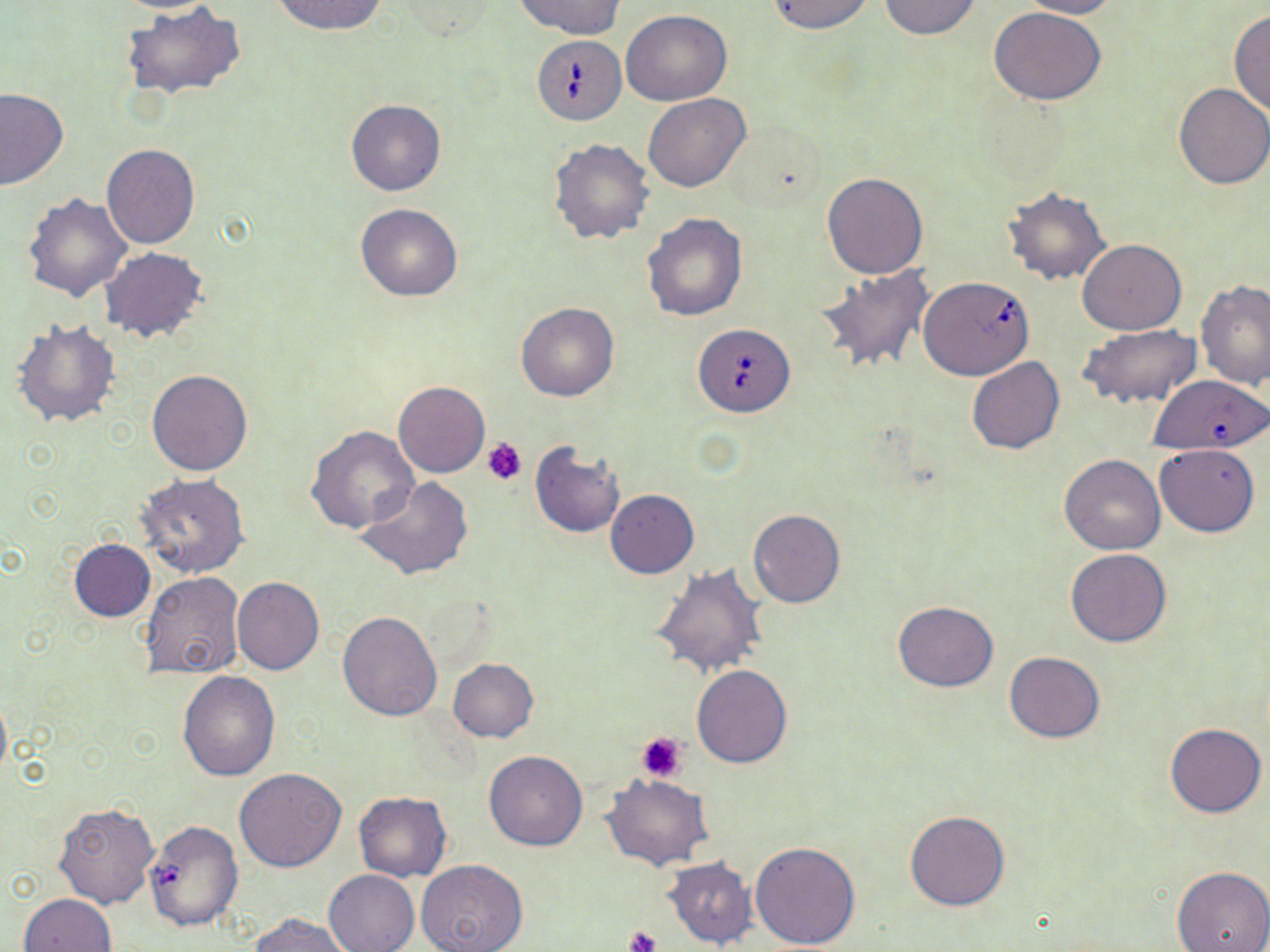

slide_level_diagnosis: Babesia divergens
stain: May-Grünwald-Giemsa
modality: optical microscopy
image_size: 1270×952 pixels
platelet_locations: 'approximate bounding boxes as named x1/y1/x2/y2 corners in pixels: (x1=484, y1=438, x2=528, y2=485), (x1=637, y1=732, x2=688, y2=781), (x1=626, y1=925, x2=662, y2=952)'
babesia_divergens_infected_red_blood_cell_locations: 'approximate bounding boxes as named x1/y1/x2/y2 corners in pixels: (x1=531, y1=35, x2=625, y2=124), (x1=920, y1=277, x2=1033, y2=380), (x1=694, y1=324, x2=796, y2=416), (x1=1147, y1=378, x2=1270, y2=457), (x1=145, y1=822, x2=243, y2=932)'
field_of_view: one of a larger specimen
uninfected_red_blood_cell_locations: 'approximate bounding boxes as named x1/y1/x2/y2 corners in pixels: (x1=106, y1=0, x2=226, y2=13), (x1=271, y1=0, x2=388, y2=36), (x1=517, y1=0, x2=624, y2=39), (x1=767, y1=0, x2=875, y2=35), (x1=877, y1=0, x2=983, y2=41), (x1=1017, y1=0, x2=1122, y2=19), (x1=119, y1=1, x2=247, y2=101), (x1=388, y1=1, x2=499, y2=41), (x1=990, y1=7, x2=1107, y2=106), (x1=621, y1=9, x2=731, y2=105), (x1=1229, y1=10, x2=1270, y2=118), (x1=1173, y1=83, x2=1270, y2=189), (x1=0, y1=88, x2=67, y2=190), (x1=643, y1=93, x2=750, y2=193), (x1=346, y1=99, x2=447, y2=196), (x1=548, y1=137, x2=655, y2=244), (x1=101, y1=144, x2=200, y2=249), (x1=822, y1=172, x2=928, y2=279), (x1=1001, y1=185, x2=1111, y2=285), (x1=23, y1=192, x2=132, y2=303), (x1=354, y1=203, x2=463, y2=301), (x1=642, y1=212, x2=747, y2=320), (x1=1077, y1=238, x2=1186, y2=335), (x1=100, y1=247, x2=208, y2=342), (x1=815, y1=265, x2=935, y2=376), (x1=1195, y1=280, x2=1270, y2=392), (x1=516, y1=303, x2=618, y2=402), (x1=11, y1=318, x2=122, y2=428), (x1=1081, y1=322, x2=1203, y2=408), (x1=967, y1=357, x2=1064, y2=454), (x1=147, y1=369, x2=253, y2=476), (x1=392, y1=381, x2=489, y2=478), (x1=306, y1=424, x2=419, y2=534), (x1=529, y1=442, x2=625, y2=537), (x1=1155, y1=443, x2=1259, y2=536), (x1=1060, y1=455, x2=1165, y2=554), (x1=137, y1=473, x2=249, y2=578), (x1=357, y1=477, x2=475, y2=581), (x1=606, y1=490, x2=699, y2=578), (x1=748, y1=509, x2=844, y2=608), (x1=68, y1=538, x2=156, y2=622), (x1=1066, y1=548, x2=1171, y2=646), (x1=651, y1=563, x2=768, y2=679), (x1=139, y1=571, x2=246, y2=680), (x1=231, y1=576, x2=324, y2=675), (x1=892, y1=601, x2=999, y2=691), (x1=337, y1=610, x2=443, y2=721), (x1=1003, y1=651, x2=1105, y2=743), (x1=447, y1=657, x2=538, y2=741), (x1=691, y1=665, x2=793, y2=768), (x1=177, y1=670, x2=281, y2=780), (x1=1165, y1=722, x2=1266, y2=818), (x1=483, y1=750, x2=588, y2=851), (x1=234, y1=768, x2=347, y2=872), (x1=602, y1=774, x2=711, y2=870), (x1=353, y1=792, x2=452, y2=882), (x1=51, y1=801, x2=159, y2=908), (x1=905, y1=809, x2=1011, y2=912), (x1=751, y1=841, x2=860, y2=949), (x1=662, y1=856, x2=758, y2=949), (x1=415, y1=860, x2=529, y2=952), (x1=1172, y1=864, x2=1270, y2=952), (x1=324, y1=868, x2=420, y2=952), (x1=18, y1=893, x2=117, y2=952), (x1=247, y1=912, x2=352, y2=952)'
magnification: 1000x
preparation: thin blood smear